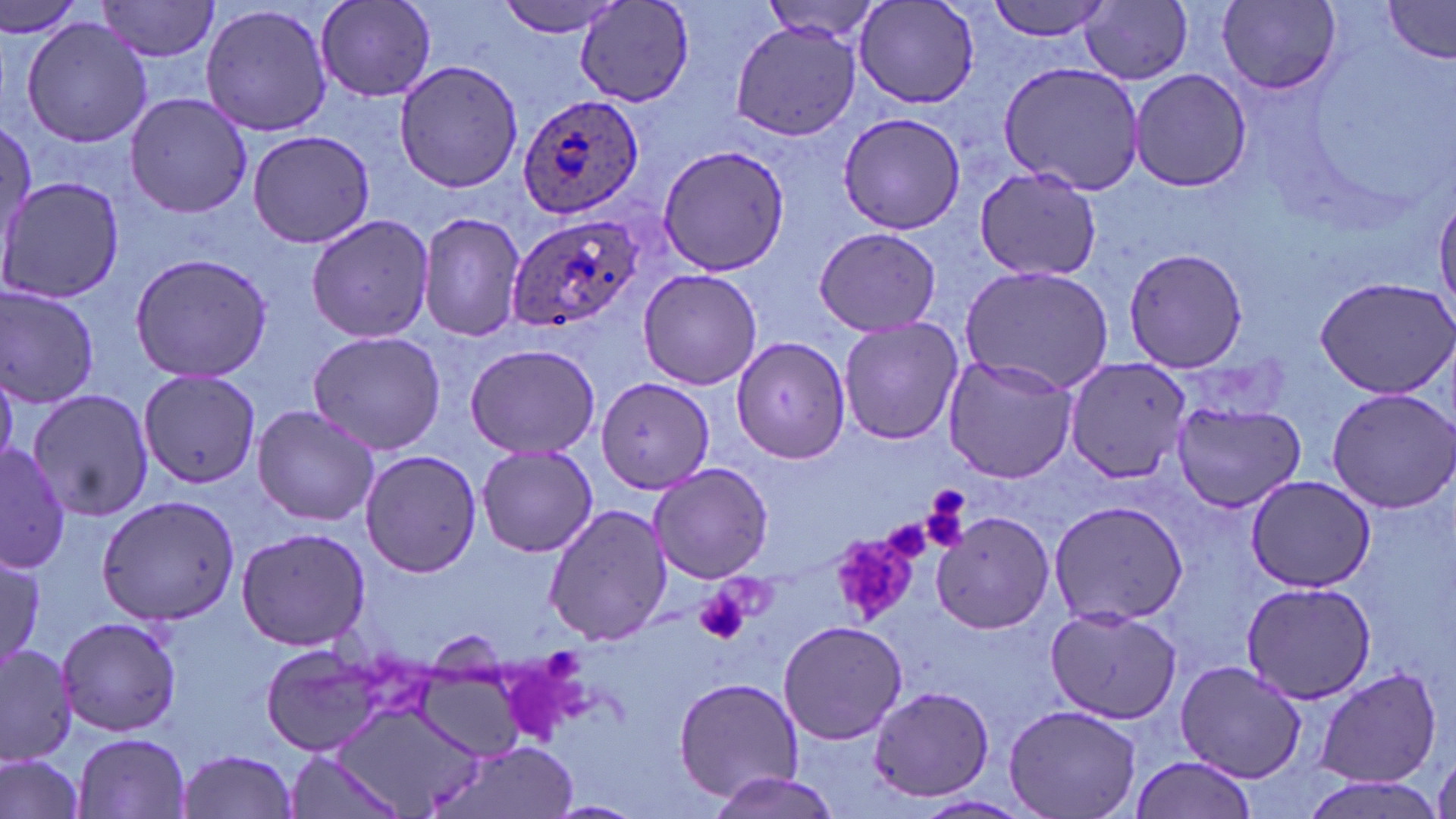
slide-level diagnosis = Plasmodium ovale
modality = light microscopy
magnification = 1000x
image size = 1456×819 pixels
uninfected red blood cell locations = approximate bounding boxes as named x1/y1/x2/y2 corners in pixels: (x1=0, y1=0, x2=89, y2=43), (x1=95, y1=0, x2=223, y2=62), (x1=314, y1=0, x2=437, y2=103), (x1=498, y1=0, x2=628, y2=38), (x1=756, y1=0, x2=888, y2=44), (x1=983, y1=0, x2=1115, y2=42), (x1=1082, y1=0, x2=1193, y2=85), (x1=575, y1=1, x2=696, y2=107), (x1=1383, y1=1, x2=1456, y2=62), (x1=199, y1=2, x2=336, y2=137), (x1=854, y1=2, x2=981, y2=109), (x1=1217, y1=2, x2=1343, y2=94), (x1=21, y1=17, x2=152, y2=148), (x1=731, y1=22, x2=859, y2=139), (x1=392, y1=59, x2=526, y2=193), (x1=996, y1=62, x2=1143, y2=195), (x1=1129, y1=69, x2=1249, y2=192), (x1=124, y1=92, x2=253, y2=219), (x1=839, y1=113, x2=965, y2=234), (x1=0, y1=116, x2=34, y2=253), (x1=245, y1=128, x2=379, y2=247), (x1=655, y1=143, x2=791, y2=278), (x1=974, y1=167, x2=1101, y2=281), (x1=2, y1=175, x2=122, y2=305), (x1=1434, y1=191, x2=1456, y2=321), (x1=417, y1=209, x2=526, y2=344), (x1=304, y1=212, x2=436, y2=345), (x1=814, y1=226, x2=942, y2=338), (x1=1121, y1=245, x2=1250, y2=373), (x1=129, y1=251, x2=273, y2=385), (x1=957, y1=265, x2=1115, y2=394), (x1=637, y1=269, x2=765, y2=390), (x1=1314, y1=274, x2=1456, y2=399), (x1=0, y1=284, x2=102, y2=409), (x1=837, y1=317, x2=964, y2=446), (x1=306, y1=329, x2=447, y2=456), (x1=731, y1=333, x2=851, y2=462), (x1=464, y1=341, x2=602, y2=460), (x1=941, y1=355, x2=1077, y2=484), (x1=1064, y1=359, x2=1191, y2=484), (x1=138, y1=369, x2=261, y2=491), (x1=594, y1=378, x2=713, y2=493), (x1=1326, y1=387, x2=1456, y2=512), (x1=25, y1=388, x2=152, y2=523), (x1=1171, y1=401, x2=1307, y2=513), (x1=251, y1=403, x2=380, y2=529), (x1=0, y1=442, x2=73, y2=572), (x1=476, y1=445, x2=597, y2=558), (x1=359, y1=449, x2=485, y2=578), (x1=647, y1=462, x2=773, y2=584), (x1=1245, y1=474, x2=1376, y2=592), (x1=96, y1=494, x2=241, y2=625), (x1=1047, y1=501, x2=1189, y2=626), (x1=543, y1=502, x2=672, y2=647), (x1=930, y1=512, x2=1055, y2=635), (x1=234, y1=526, x2=372, y2=650), (x1=1, y1=557, x2=47, y2=661), (x1=1238, y1=580, x2=1379, y2=703), (x1=1044, y1=605, x2=1182, y2=723), (x1=56, y1=613, x2=184, y2=739), (x1=777, y1=620, x2=909, y2=745), (x1=0, y1=642, x2=79, y2=766), (x1=258, y1=643, x2=386, y2=758), (x1=1176, y1=660, x2=1308, y2=782), (x1=1314, y1=667, x2=1443, y2=786), (x1=674, y1=674, x2=803, y2=802), (x1=866, y1=686, x2=997, y2=803), (x1=1004, y1=703, x2=1142, y2=818), (x1=328, y1=704, x2=492, y2=817), (x1=73, y1=732, x2=193, y2=818), (x1=431, y1=743, x2=579, y2=819), (x1=176, y1=750, x2=299, y2=819), (x1=0, y1=751, x2=87, y2=819), (x1=287, y1=755, x2=406, y2=819), (x1=1126, y1=755, x2=1260, y2=819), (x1=707, y1=771, x2=838, y2=819), (x1=1297, y1=774, x2=1448, y2=819), (x1=911, y1=796, x2=1034, y2=819)
stain = May-Grünwald-Giemsa
platelet locations = approximate bounding boxes as named x1/y1/x2/y2 corners in pixels: (x1=919, y1=492, x2=972, y2=554), (x1=882, y1=516, x2=937, y2=563), (x1=831, y1=523, x2=929, y2=618), (x1=695, y1=586, x2=750, y2=646)
field of view = single
Plasmodium ovale-infected red blood cell locations = approximate bounding boxes as named x1/y1/x2/y2 corners in pixels: (x1=511, y1=90, x2=648, y2=220), (x1=505, y1=211, x2=645, y2=337)
preparation = thin blood film